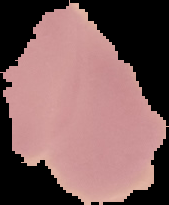

Image is 169×205 pixels. Malaria status: uninfected. From a thin blood smear. Segmented cell region on a black background.